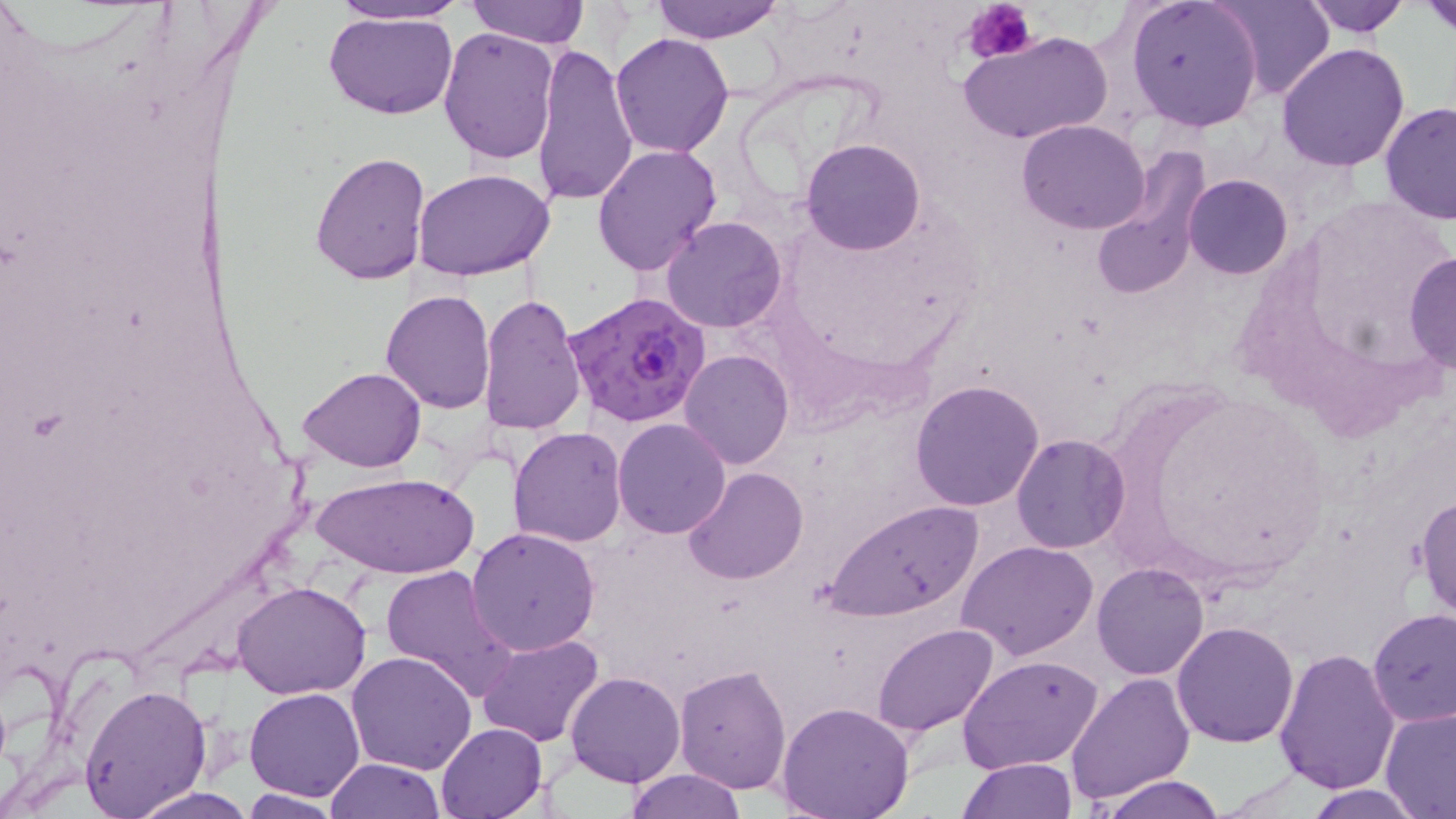
Summary:
  - Coordinate format: approximate bounding boxes as [x1, y1, x2, y2] in pixels
  - Plasmodium falciparum-infected red blood cell locations: [564, 291, 715, 428]
  - Uninfected red blood cell locations: [325, 0, 466, 26], [467, 0, 587, 48], [651, 0, 786, 42], [1124, 0, 1263, 131], [1298, 0, 1412, 37], [1421, 0, 1456, 36], [1207, 2, 1334, 98], [322, 10, 459, 120], [437, 28, 560, 163], [960, 29, 1112, 147], [610, 32, 736, 156], [530, 40, 639, 210], [1276, 43, 1410, 173], [1379, 103, 1456, 226], [1016, 119, 1151, 235], [802, 138, 926, 255], [591, 143, 723, 275], [1089, 147, 1212, 304], [309, 151, 431, 284], [412, 168, 556, 279], [1184, 173, 1294, 280], [662, 215, 786, 333], [1405, 253, 1456, 373], [381, 289, 496, 413], [479, 293, 587, 437], [679, 350, 794, 470], [299, 367, 425, 473], [910, 378, 1044, 511], [611, 419, 732, 539], [507, 426, 630, 548], [1010, 432, 1129, 552], [683, 465, 807, 584], [312, 470, 479, 581], [1411, 492, 1456, 619], [823, 500, 982, 620], [466, 526, 600, 654], [958, 540, 1098, 660], [380, 564, 519, 700], [1092, 564, 1209, 680], [233, 582, 371, 699], [1367, 609, 1456, 728], [1171, 621, 1299, 748], [873, 623, 998, 734], [476, 633, 603, 749], [1274, 646, 1401, 794], [346, 651, 477, 774], [957, 653, 1105, 772], [674, 664, 791, 793], [1065, 670, 1195, 803], [564, 672, 685, 788], [78, 681, 210, 816], [245, 686, 364, 801], [775, 701, 916, 819], [1379, 707, 1456, 817], [435, 722, 547, 818], [325, 757, 446, 818], [958, 758, 1075, 818], [624, 768, 747, 819], [1099, 775, 1229, 819], [1299, 787, 1432, 818], [125, 788, 257, 818], [238, 791, 347, 817]
  - Platelet locations: [962, 0, 1036, 65]
  - Slide-level diagnosis: Plasmodium falciparum
  - Modality: optical microscopy
  - Magnification: 1000x
  - Image size: 1456×819 pixels
  - Stain: May-Grünwald-Giemsa
  - Preparation: thin blood film
  - Field of view: single